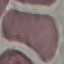 Malaria status: uninfected. Cell patch, automatically extracted from a larger field of view and resized to 64 × 64 pixels. Acquired by smartphone through the microscope eyepiece. Thin smear of blood. Giemsa stain.